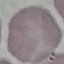

Summary:
  - Malaria status: uninfected
  - Capture: smartphone camera at the microscope eyepiece
  - Image type: cell patch, automatically extracted from a larger field of view and resized to 64 × 64 pixels
  - Stain: Giemsa
  - Preparation: thin blood smear